State which parasite is depicted.
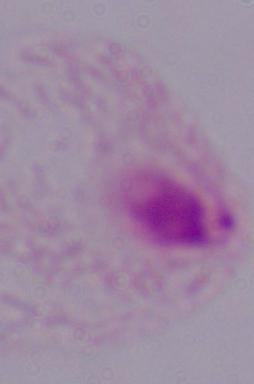

A trichomonad.

Micrograph. Captured at 1000x magnification.